Locate every malaria parasite.
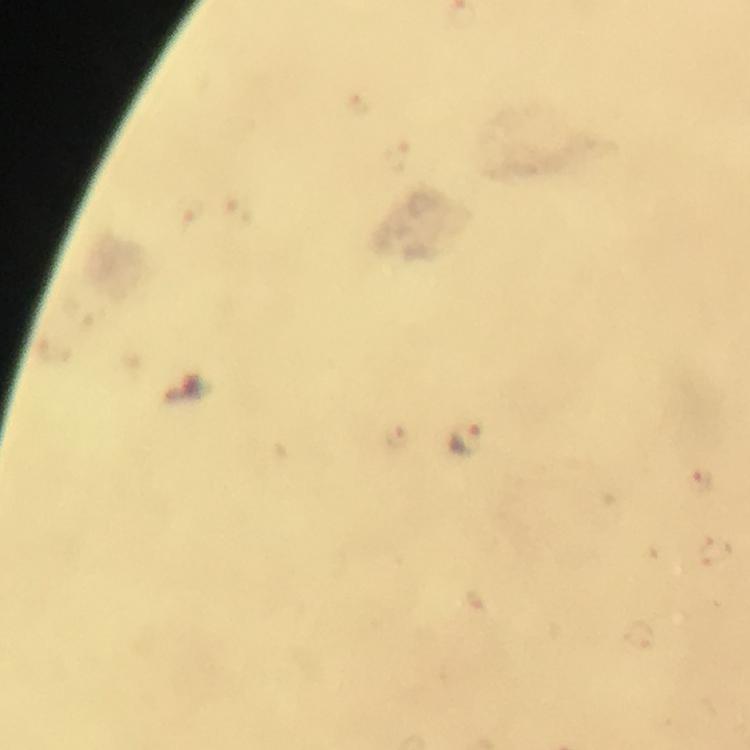

Approximate object centers, in pixels from the top-left corner.
Malaria parasites: (x=398, y=159), (x=468, y=443), (x=699, y=483).

Summary:
  - Immersion oil: used
  - Stain: Giemsa
  - Image size: 750×750 pixels
  - Preparation: thick blood smear
  - Cropped from: a single field of view
  - Context: from a malaria diagnostic workup
  - Magnification: 100x
  - Capture: smartphone photograph through a microscope